Locate every malaria parasite.
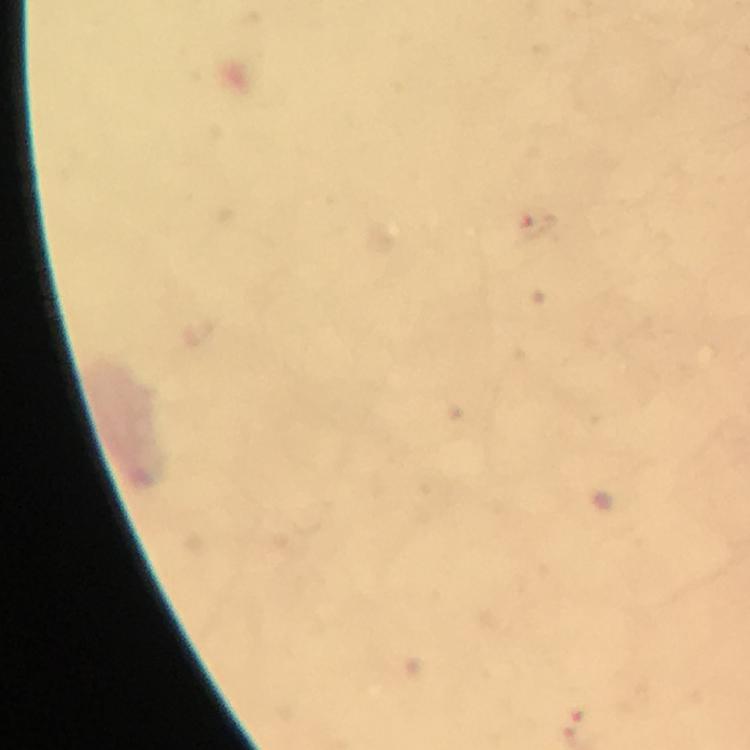
Approximate centers as (x, y) in pixels.
Malaria parasites: (582, 709).

Summary:
  - Context: from a malaria diagnostic workup
  - Immersion oil: applied
  - Cropped from: a single field of view
  - Preparation: thick smear
  - Image size: 750×750 pixels
  - Capture: smartphone mounted on the microscope
  - Magnification: 100x
  - Stain: Giemsa